Outline each uninfected red blood cell.
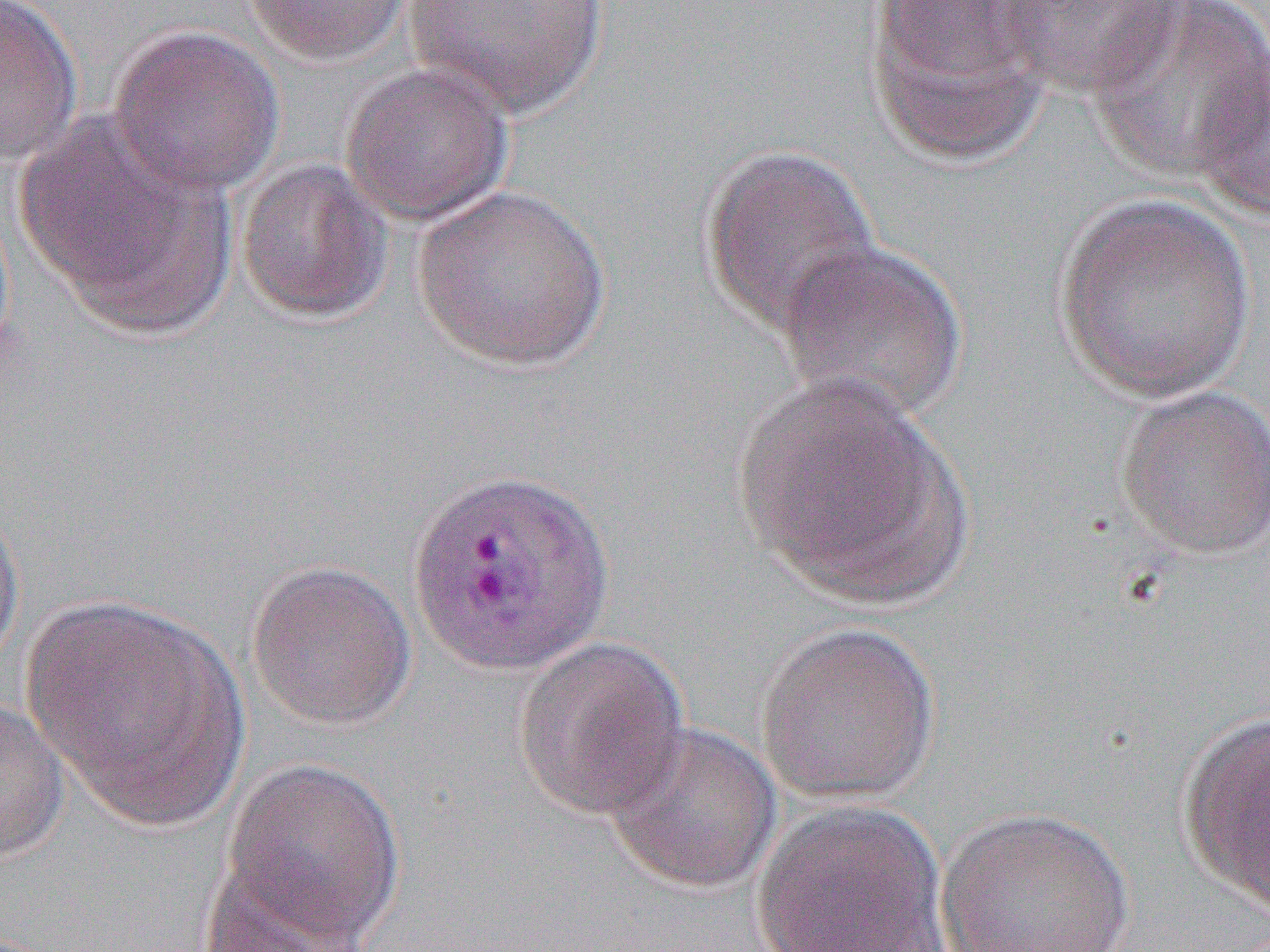

Approximate bounding boxes as [x1, y1, x2, y2] in pixels.
Uninfected red blood cells: [0, 0, 84, 168], [241, 0, 414, 65], [401, 0, 610, 119], [988, 0, 1186, 100], [1085, 2, 1268, 184], [864, 3, 1055, 165], [107, 24, 285, 198], [1192, 51, 1270, 223], [339, 63, 515, 225], [18, 115, 234, 335], [700, 145, 882, 338], [236, 158, 393, 325], [412, 185, 611, 371], [1052, 193, 1257, 403], [775, 238, 970, 425], [730, 373, 969, 608], [1113, 385, 1270, 561], [0, 493, 26, 677], [244, 558, 417, 732], [23, 594, 248, 829], [755, 621, 941, 805], [511, 635, 691, 822], [0, 696, 68, 867], [1176, 711, 1270, 914], [603, 722, 782, 895], [219, 756, 407, 945], [748, 802, 951, 951], [934, 808, 1136, 952], [196, 868, 380, 951].

{
  "slide_level_diagnosis": "Plasmodium vivax",
  "preparation": "thin blood film",
  "image_size": "1270×952 pixels",
  "magnification": "1000x",
  "field_of_view": "single",
  "modality": "optical microscopy"
}